State which parasite is depicted.
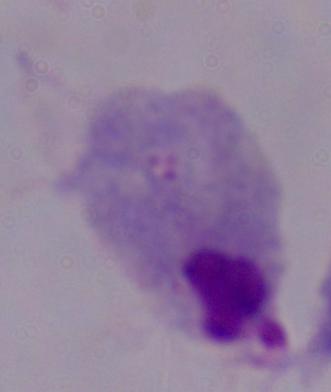

This is a trichomonad.

Summary:
  - Modality: micrograph
  - Magnification: 1000x